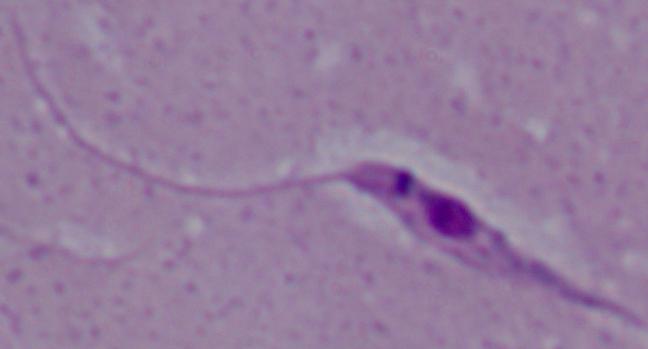 Captured at 1000x magnification. A Leishmania parasite is shown. Photomicrograph.